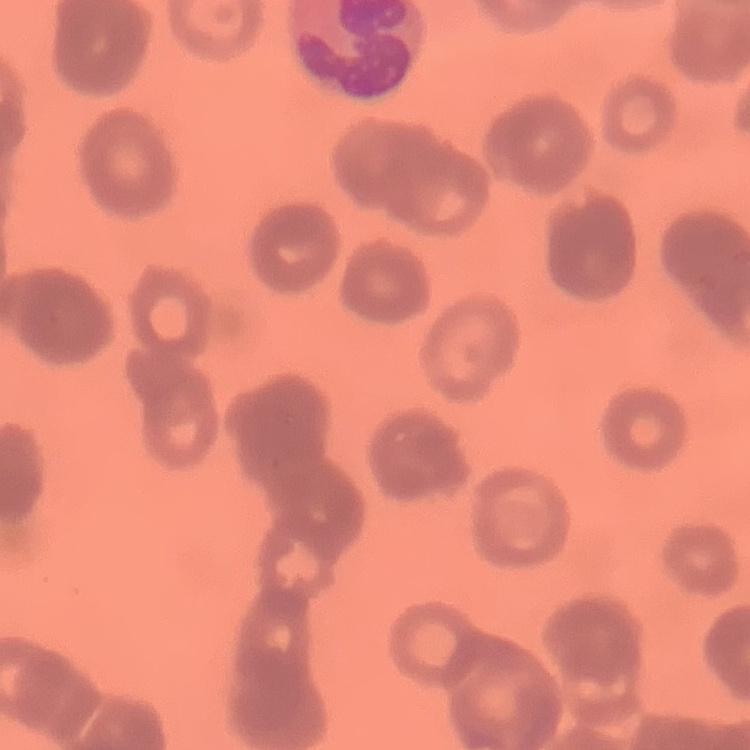

red blood cell morphology = rouleaux formation
preparation = thin blood smear
stain = Field's or Giemsa
image type = one tile cut from a larger photomicrograph